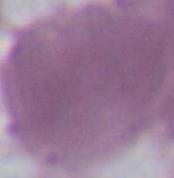

Photomicrograph. An erythrocyte is shown. 1000x magnification.